State which parasite is depicted.
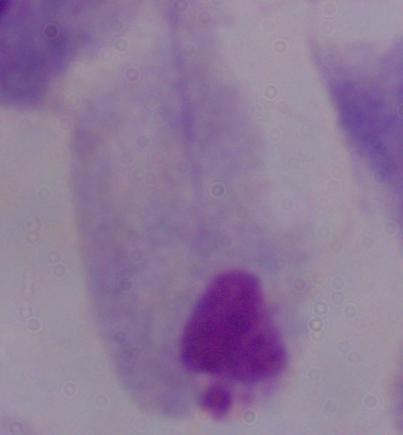

A trichomonad.

1000x magnification. Photomicrograph.